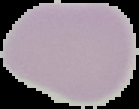
The area outside the segmented cell region is set to black. From a thin blood smear. Malaria status: uninfected. Image is 139×109 pixels.